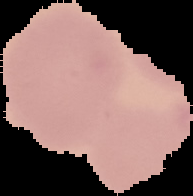
malaria status = uninfected
image size = 193×196 pixels
image type = segmented cell region on a black background
preparation = thin blood film